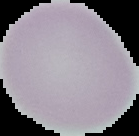

Image is 139×136 pixels. Segmented cell region on a black background. From a thin blood smear. Malaria status: uninfected.